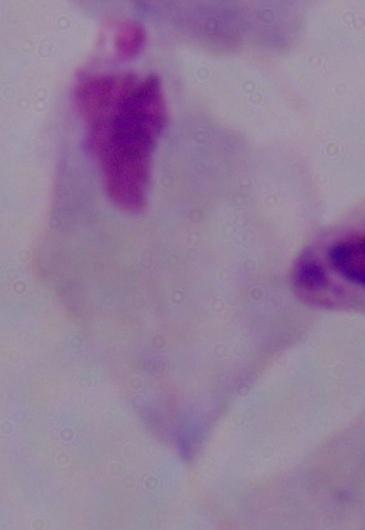 A trichomonad is shown. Photomicrograph. Captured at 1000x magnification.